Comment on the morphology of the erythrocytes.
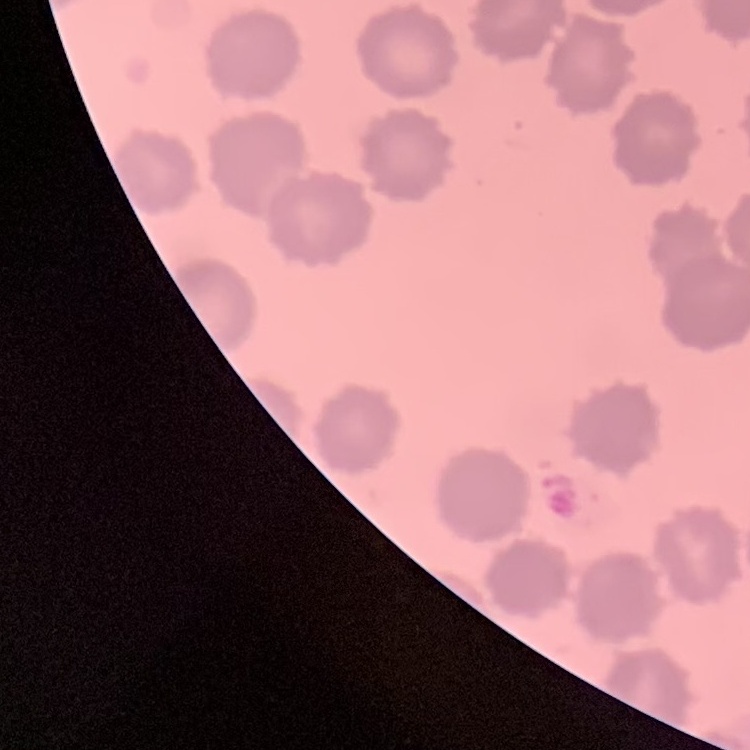
No rouleaux formation.

One tile cut from a larger photomicrograph. Field's or Giemsa stain. Thin blood smear.